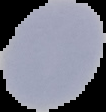

Summary:
  - Preparation: thin blood film
  - Malaria status: uninfected
  - Image type: segmented cell region on a black background
  - Image size: 106×112 pixels